State which cell type is depicted.
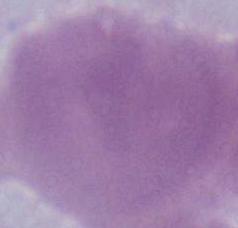
This is an erythrocyte.

Summary:
  - Magnification: 1000x
  - Modality: micrograph